Locate every Plasmodium parasite.
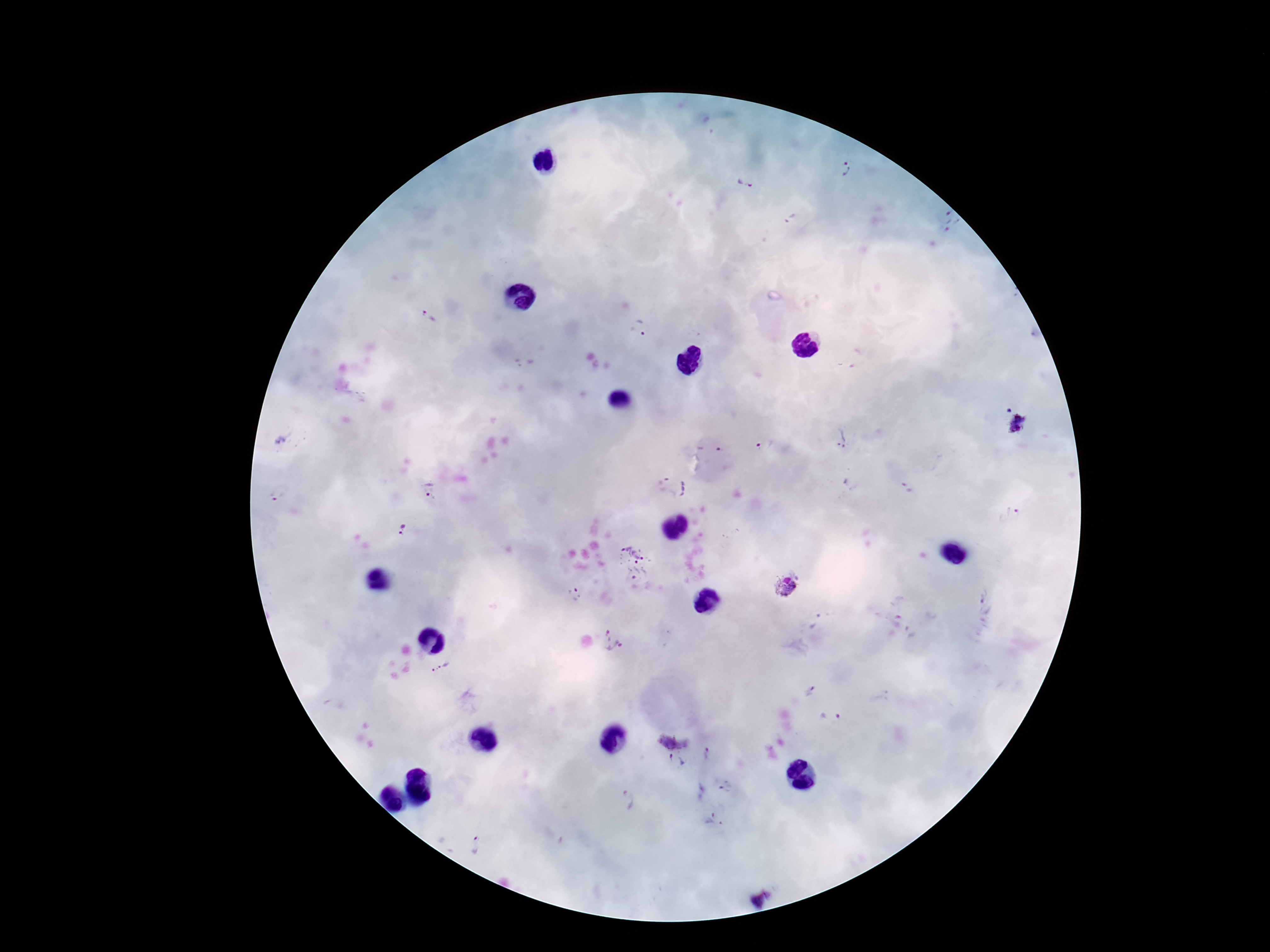

Approximate centers as [x, y] in pixels.
Plasmodium parasites: [846, 169], [745, 185], [950, 221], [429, 319], [639, 328], [1018, 426], [843, 438], [282, 440], [766, 446], [908, 487], [430, 492], [278, 496], [1009, 513], [404, 529], [632, 555], [635, 577], [786, 586], [575, 595], [613, 638], [440, 668], [832, 717], [676, 729], [708, 755], [675, 763], [725, 788], [626, 799], [711, 820], [481, 844].

magnification = 100x
patient malaria status = infected
capture = smartphone camera through the microscope eyepiece
image size = 1270×952 pixels
field of view = single
preparation = thick blood film
stain = Giemsa